Assess for parasitized red blood cells.
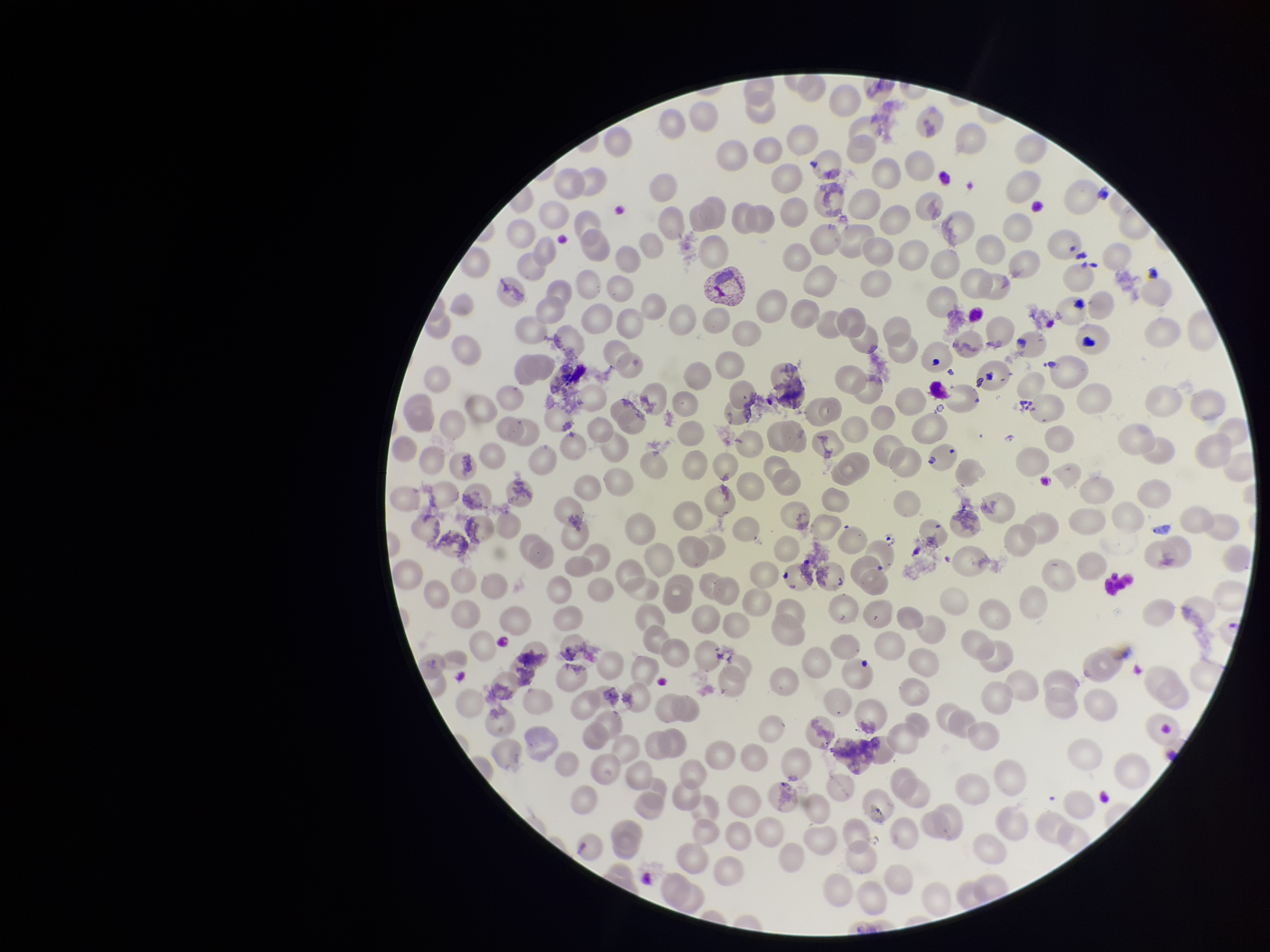

None identified.

Red blood cell count: 254. Patient malaria status: positive. Single field of view. Giemsa stain. Preparation: thin smear. Photographed through the microscope eyepiece with a smartphone camera. Parasitized red blood cell count: 0. Image is 1270×952 pixels. Species reported for this patient: Plasmodium vivax.